Assess this cell for malaria.
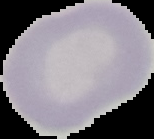
It is uninfected.

Summary:
  - Image type: cell region segmented out of the field of view; surrounding area masked to black
  - Preparation: thin blood smear
  - Image size: 154×139 pixels